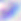
identification = Toxoplasma gondii
modality = micrograph
magnification = 400x